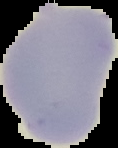
Summary:
  - Image size: 118×148 pixels
  - Image type: segmented cell region with the area outside set to black
  - Result: no Plasmodium parasites detected
  - Preparation: thin blood film